Describe the morphology of the erythrocytes.
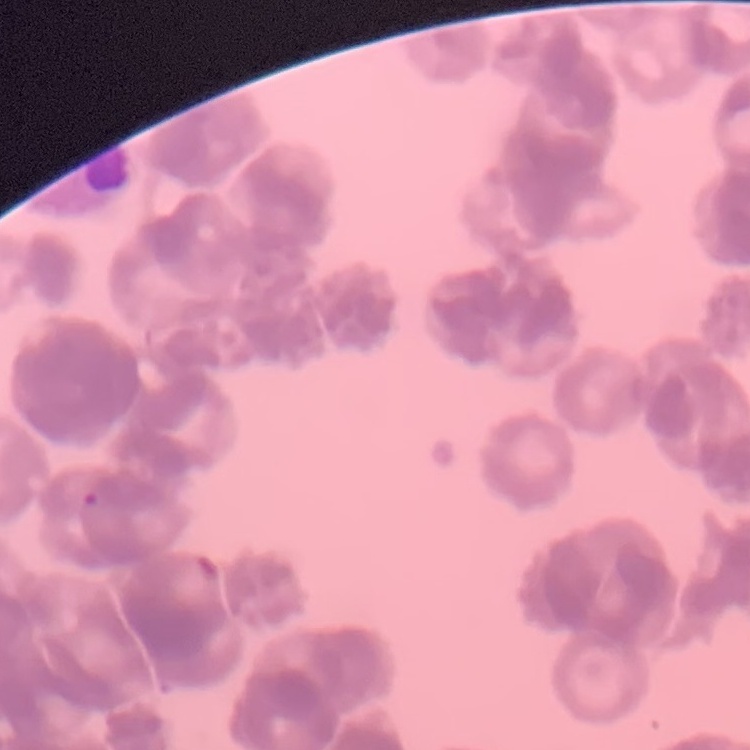

They show rouleaux formation.

Square crop of a larger photomicrograph. Thin blood smear. Field's or Giemsa stain.